Report the malaria status of this cell.
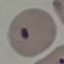

Parasitized.

Summary:
  - Stain: Giemsa
  - Image type: cell patch, automatically extracted from a larger field of view and resized to 64 × 64 pixels
  - Capture: smartphone camera at the microscope eyepiece
  - Preparation: thin blood smear